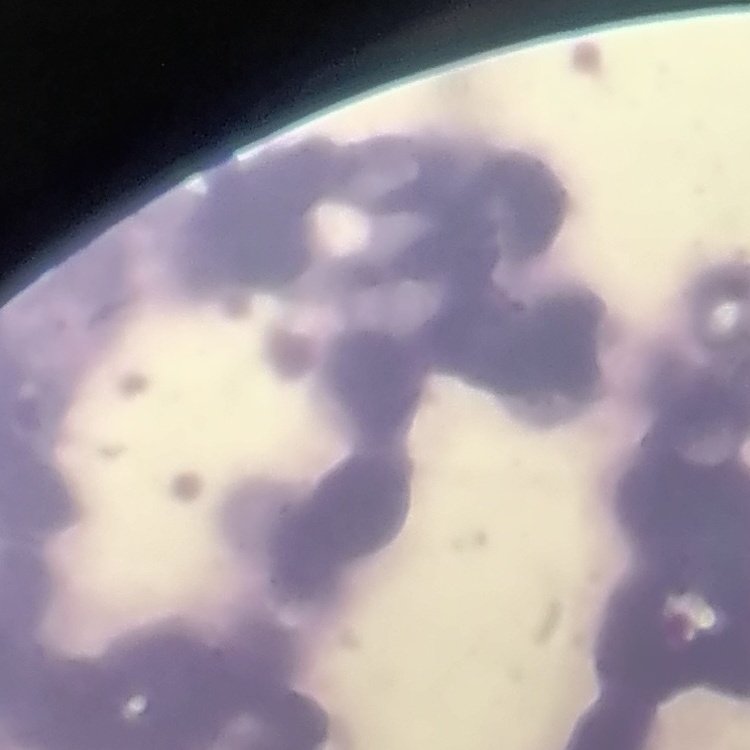 The red blood cells exhibit rouleaux formation. Square crop of a larger photomicrograph. Field's or Giemsa stain. Thin blood film.